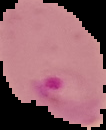
result = malaria parasites identified
image type = cell region segmented out of the field of view; surrounding area masked to black
preparation = thin blood film
image size = 106×130 pixels